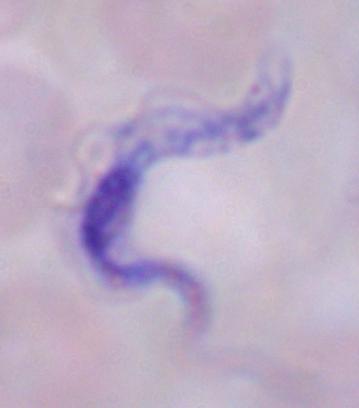

Photomicrograph. A trypanosome is shown. Captured at 1000x magnification.